Report the malaria status of this cell.
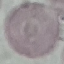

Uninfected.

Summary:
  - Stain: Giemsa
  - Preparation: thin smear
  - Capture: smartphone camera at the microscope eyepiece
  - Image type: automatically extracted cell patch, resized to 64 × 64 pixels